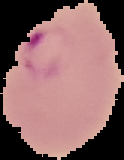

preparation = thin blood smear
malaria status = parasitized
image size = 124×160 pixels
image type = segmented cell region with the area outside set to black